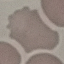

Summary:
  - Malaria status: uninfected
  - Preparation: thin blood film
  - Stain: Giemsa
  - Image type: automatically extracted cell patch, resized to 64 × 64 pixels
  - Capture: smartphone through the microscope eyepiece